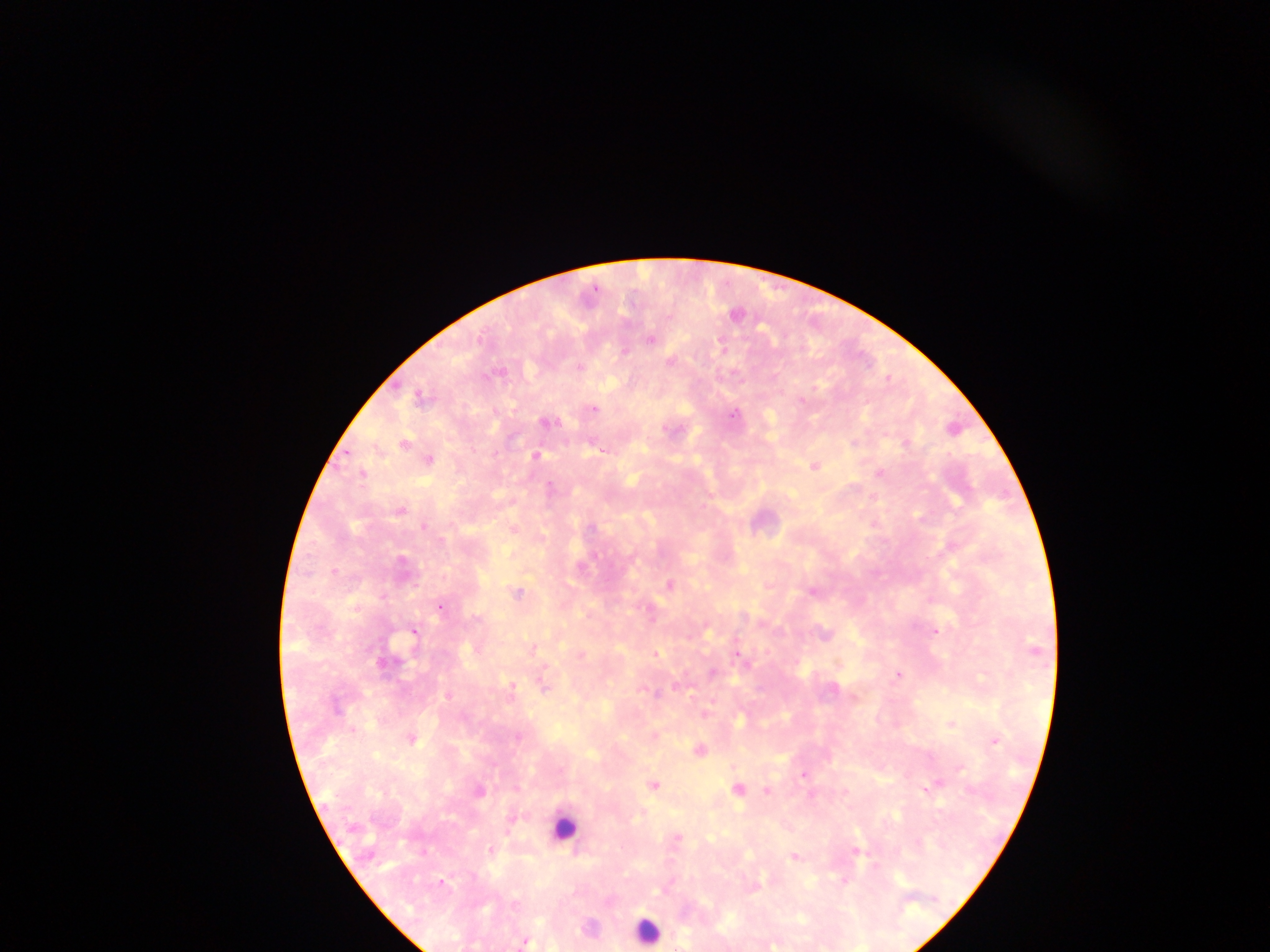

Approximate centers as x y in pixels.
Summary:
  - Leukocyte locations: 564 828; 646 930
  - Plasmodium parasite locations: 650 340; 624 351; 669 362; 579 366; 419 397; 594 409; 734 414; 546 422; 404 444; 600 450; 536 456; 428 460; 814 467; 880 473; 363 474; 550 487; 400 511; 425 527; 591 527; 443 540; 594 555; 402 561; 334 571; 670 585; 811 591; 517 593; 383 598; 439 607; 650 611; 477 620; 935 631; 413 632; 824 635; 533 649; 1034 650; 656 653; 737 654; 386 664; 712 673; 897 675; 511 686; 542 686; 677 687; 655 693; 447 696; 855 697; 335 706; 706 713; 950 724; 518 737; 411 739; 995 741; 699 750; 960 768; 803 775; 934 785; 653 786; 926 788; 737 789; 767 791; 479 792; 812 796; 512 818; 678 838; 492 849; 855 851; 794 857; 844 881; 441 882; 753 886; 515 905; 524 942
  - Field of view: single
  - Capture: mobile-phone photograph through a microscope
  - Preparation: thick blood smear
  - Country: Ghana
  - Image size: 1270×952 pixels